Outline each blood parasite and name the species.
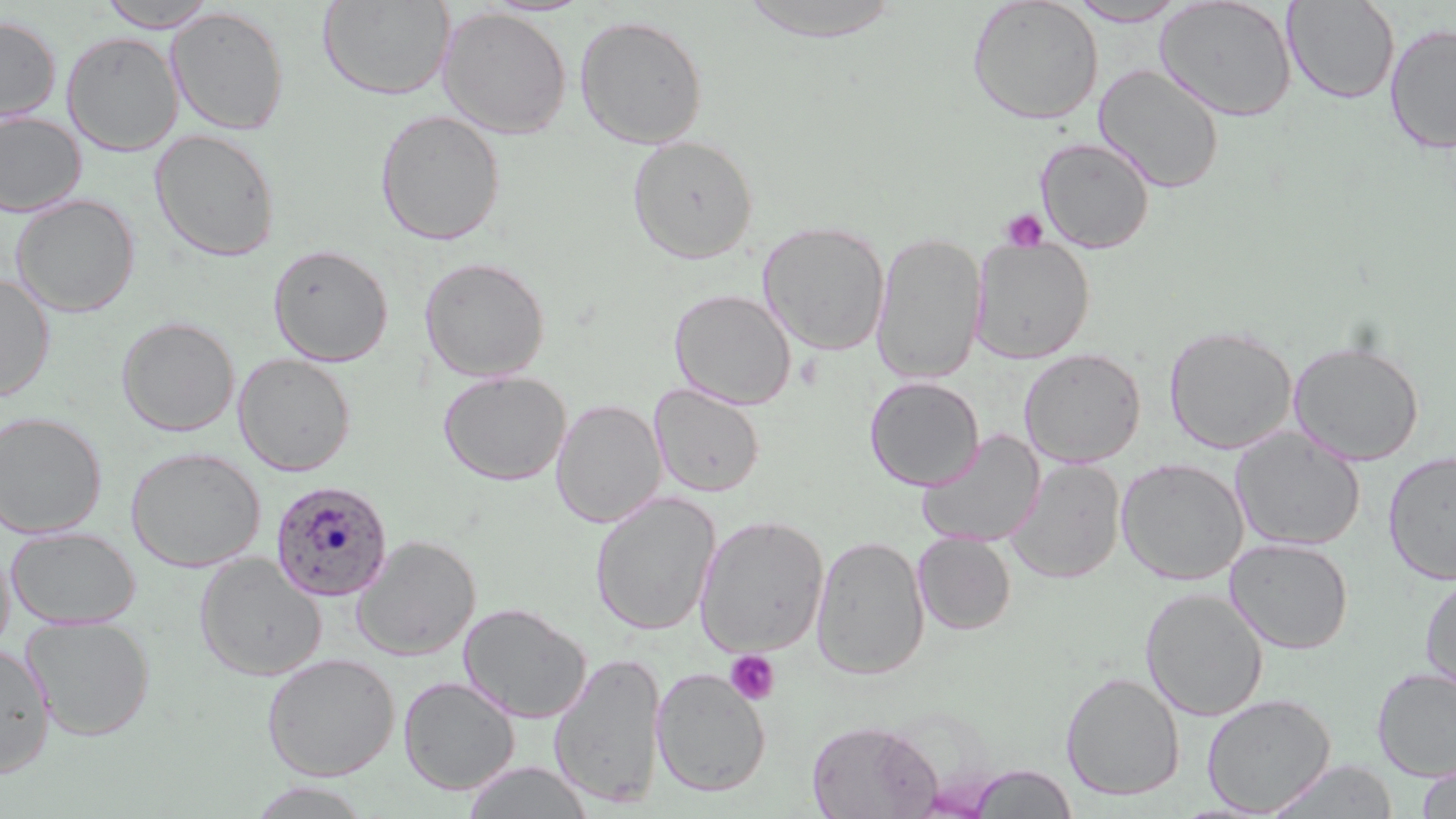

Approximate bounding boxes as (x1,y1)-(x2,y2) corner pairs in pixels.
Plasmodium ovale-infected red blood cells: (269,480)-(394,602).
No Plasmodium falciparum, Plasmodium malariae, Plasmodium vivax, Babesia divergens, or Trypanosoma brucei observed.

Platelet locations: (1001,208)-(1049,252), (725,649)-(781,704). Uninfected red blood cell locations: (318,0)-(454,101), (738,0)-(905,43), (966,0)-(1104,126), (1154,0)-(1298,122), (1283,0)-(1400,104), (96,1)-(220,32), (1065,1)-(1191,26), (167,6)-(289,136), (437,6)-(571,139), (574,14)-(708,149), (0,15)-(61,124), (1384,22)-(1456,155), (61,30)-(183,156), (1093,63)-(1225,194), (374,109)-(506,245), (0,111)-(87,217), (149,128)-(281,261), (627,134)-(759,264), (1035,136)-(1156,253), (11,194)-(141,318), (758,221)-(891,356), (871,231)-(987,385), (970,238)-(1095,363), (268,243)-(394,366), (419,256)-(550,382), (0,273)-(55,401), (669,288)-(797,409), (116,316)-(240,436), (1164,325)-(1298,455), (1288,338)-(1426,465), (1019,348)-(1146,468), (233,353)-(356,476), (438,369)-(572,486), (865,376)-(984,491), (649,383)-(765,497), (551,398)-(666,528), (0,411)-(107,538), (1230,427)-(1365,551), (916,430)-(1045,548), (126,446)-(265,572), (1383,451)-(1456,585), (1115,457)-(1249,585), (1007,458)-(1125,583), (589,491)-(721,636), (694,514)-(830,657), (5,526)-(141,630), (913,532)-(1016,635), (810,534)-(929,679), (351,535)-(481,660), (1226,537)-(1353,654), (193,553)-(327,681), (1420,573)-(1456,698), (1139,587)-(1269,721), (459,602)-(591,723), (21,616)-(156,741), (0,643)-(55,778), (549,651)-(668,810), (262,653)-(401,780), (651,667)-(771,797), (1372,667)-(1456,780), (1061,670)-(1185,801), (398,675)-(520,795), (1201,693)-(1336,815), (806,719)-(941,819), (1263,759)-(1398,818), (461,761)-(594,819), (968,764)-(1078,818), (1416,766)-(1456,818), (246,781)-(375,819). Slide-level diagnosis: Plasmodium ovale. Light microscopy. May-Grünwald-Giemsa stain. Thin blood film. Single field of view. Image is 1456×819 pixels. Captured at 1000x magnification.